Locate every leukocyte (white blood cell).
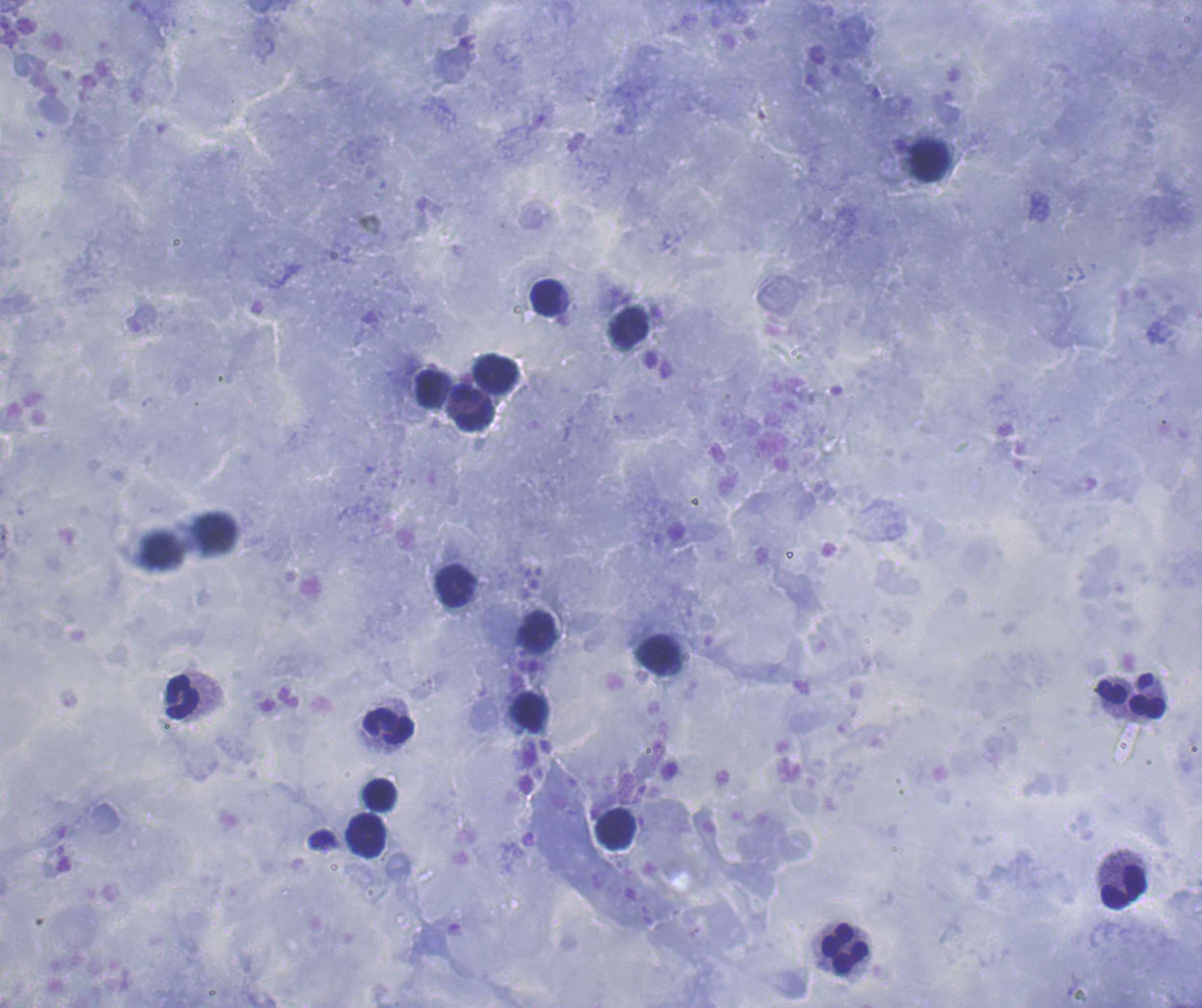
Approximate centers as [x, y] in pixels.
Leukocytes: [930, 161], [547, 298], [630, 328], [497, 372], [432, 388], [473, 407], [455, 587], [658, 654], [1111, 692], [182, 697], [1147, 708], [530, 712], [389, 727], [380, 795], [616, 828], [367, 835], [1124, 888], [845, 949].

Summary:
  - Image size: 1202×1008 pixels
  - Preparation: thick blood smear
  - Field of view: one from this slide
  - Coloration quality: good
  - Stain: Romanowsky
  - Background quality: satisfactory
  - Magnification: 100x
  - Context: previously used in an actual diagnosis
  - Result: negative for Plasmodium parasites